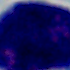
{
  "identification": "white blood cell",
  "modality": "micrograph",
  "magnification": "1000x"
}